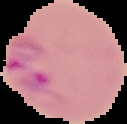

Summary:
  - Result: malaria parasites detected
  - Preparation: thin blood smear
  - Image type: cell region segmented out of the field of view; surrounding area masked to black
  - Image size: 127×124 pixels